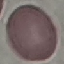
result = no malaria parasites seen
preparation = thin blood film
image type = automatically extracted cell patch, resized to 64 × 64 pixels
stain = Giemsa
capture = smartphone through the microscope eyepiece